Report the malaria status of this cell.
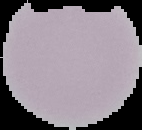

It is uninfected.

Cell region segmented out of the field of view; the surrounding area is masked to black. From a thin blood smear. Image is 142×130 pixels.